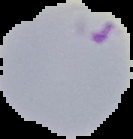
Summary:
  - Image size: 133×139 pixels
  - Image type: segmented cell region on a black background
  - Malaria status: parasitized
  - Preparation: thin blood smear